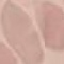
Malaria status: uninfected. Giemsa stain. Cell patch, automatically extracted from a larger field of view and resized to 64 × 64 pixels. Acquired by smartphone through the microscope eyepiece. Thin blood film.